Assess this cell for malaria.
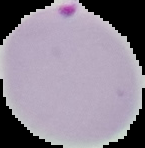
It is parasitized.

Summary:
  - Image type: segmented cell region on a black background
  - Preparation: thin blood film
  - Image size: 145×148 pixels